Assess this cell for malaria.
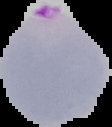
It is parasitized.

Summary:
  - Preparation: thin blood smear
  - Image size: 112×127 pixels
  - Image type: segmented cell region with the area outside set to black